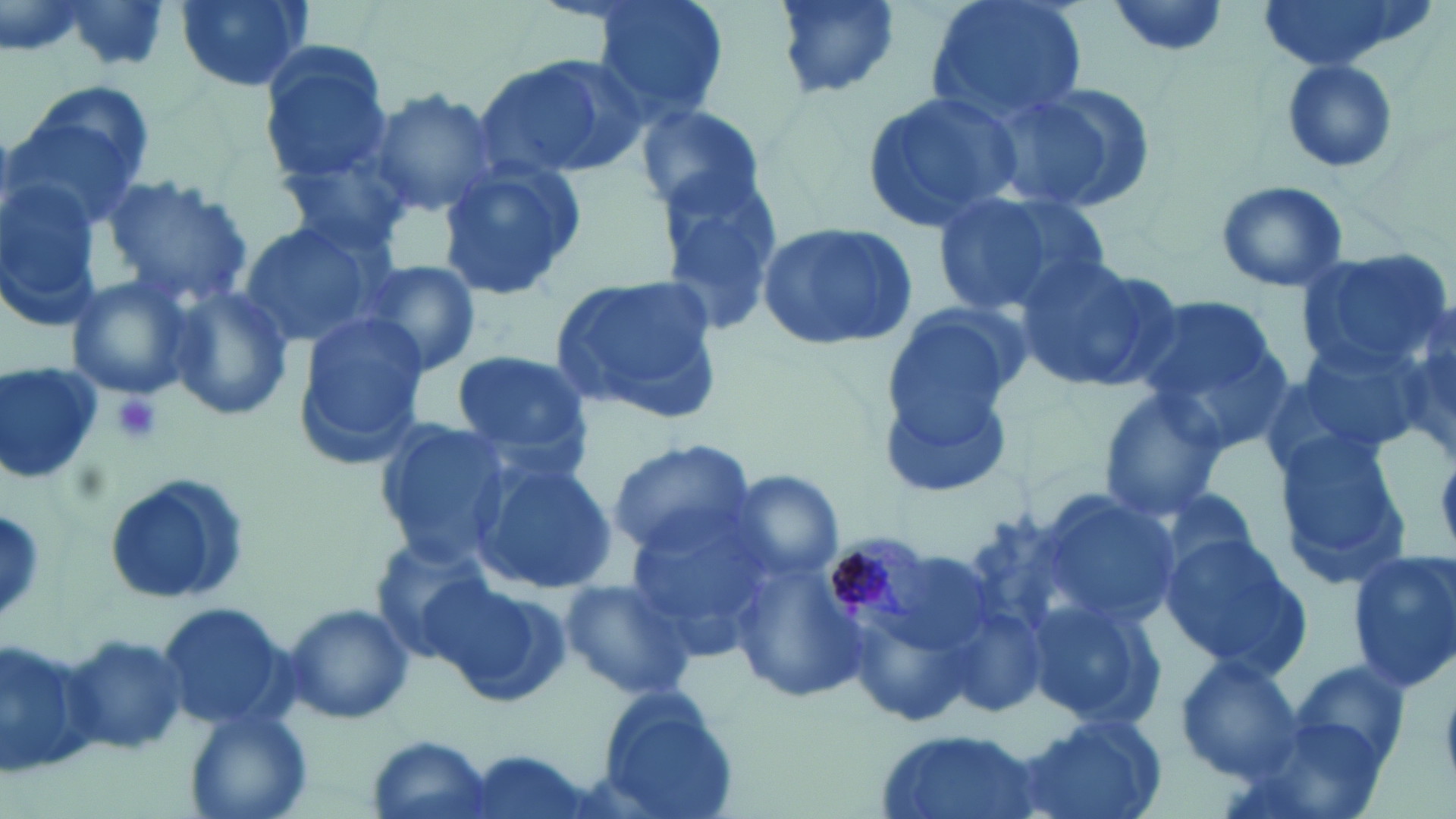
slide-level diagnosis = Plasmodium malariae
uninfected red blood cell locations = approximate bounding boxes as (x1, y1, x2, y2) in pixels: (59, 0, 179, 75), (174, 0, 315, 92), (588, 0, 731, 129), (769, 0, 904, 102), (924, 0, 1089, 129), (1255, 0, 1417, 73), (1104, 1, 1233, 59), (257, 38, 395, 185), (475, 52, 646, 181), (1281, 60, 1398, 176), (994, 82, 1156, 212), (7, 83, 152, 234), (859, 85, 1026, 231), (364, 88, 499, 217), (633, 102, 765, 218), (274, 142, 420, 263), (436, 158, 589, 302), (98, 172, 254, 308), (653, 174, 784, 336), (0, 180, 102, 324), (1214, 180, 1350, 294), (929, 189, 1100, 318), (236, 221, 384, 351), (755, 221, 918, 354), (1297, 249, 1451, 378), (1012, 253, 1179, 393), (360, 259, 482, 377), (65, 275, 197, 400), (548, 275, 725, 424), (162, 284, 297, 423), (1131, 294, 1288, 428), (1384, 300, 1456, 467), (879, 301, 1030, 485), (290, 311, 432, 467), (1273, 343, 1424, 476), (448, 349, 591, 467), (0, 358, 103, 485), (1096, 386, 1232, 520), (372, 417, 516, 563), (1272, 434, 1413, 593), (605, 439, 757, 560), (470, 457, 618, 595), (102, 471, 250, 607), (729, 472, 846, 587), (1034, 487, 1178, 634), (620, 506, 776, 652), (1159, 534, 1313, 679), (362, 539, 500, 660), (1346, 548, 1456, 693), (731, 557, 868, 705), (557, 576, 697, 702), (431, 577, 572, 706), (1025, 597, 1167, 730), (153, 599, 294, 730), (282, 602, 415, 724), (848, 614, 975, 724), (0, 632, 100, 780), (60, 635, 193, 758), (1173, 654, 1304, 780), (1290, 660, 1414, 772), (591, 683, 739, 819), (184, 708, 313, 819), (1014, 713, 1168, 819), (875, 727, 1043, 819), (366, 734, 496, 819)
Plasmodium malariae-infected red blood cell locations = approximate bounding boxes as (x1, y1, x2, y2) in pixels: (818, 533, 940, 637)
magnification = 1000x
field of view = single
preparation = thin blood film
stain = May-Grünwald-Giemsa
modality = optical microscopy
platelet locations = approximate bounding boxes as (x1, y1, x2, y2) in pixels: (111, 393, 163, 446)
image size = 1456×819 pixels